Name the parasite shown.
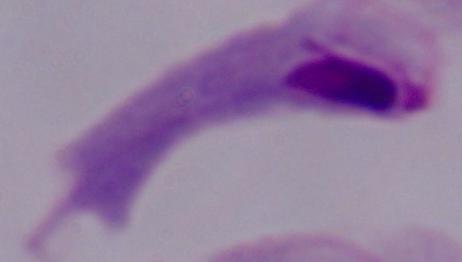

This is a trichomonad.

Summary:
  - Modality: micrograph
  - Magnification: 1000x